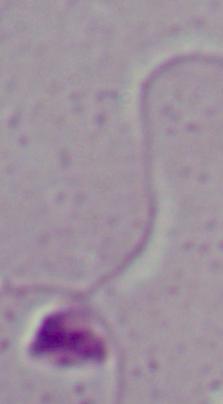
Summary:
  - Magnification: 1000x
  - Modality: photomicrograph
  - Identification: Leishmania